State which cell type is depicted.
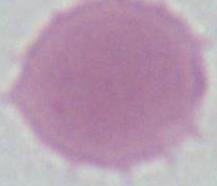

This is an erythrocyte.

magnification = 1000x
modality = micrograph